Describe the morphology of the erythrocytes.
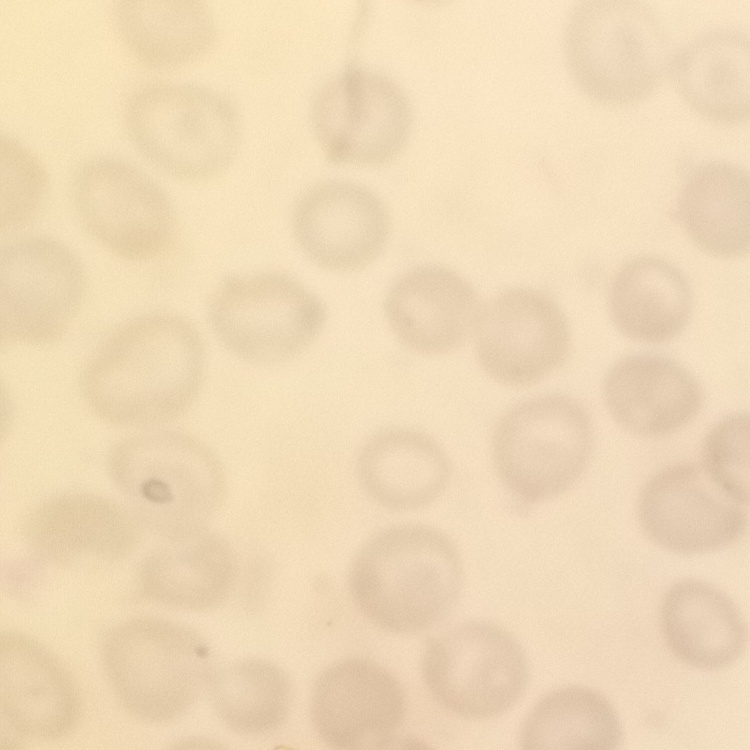
No rouleaux formation.

Thin blood film. Stained with either Field's or Giemsa. Square crop of a larger photomicrograph.